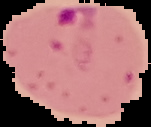
From a thin blood smear. Segmented cell region on a black background. Malaria status: parasitized. Image is 151×127 pixels.